Report the malaria status.
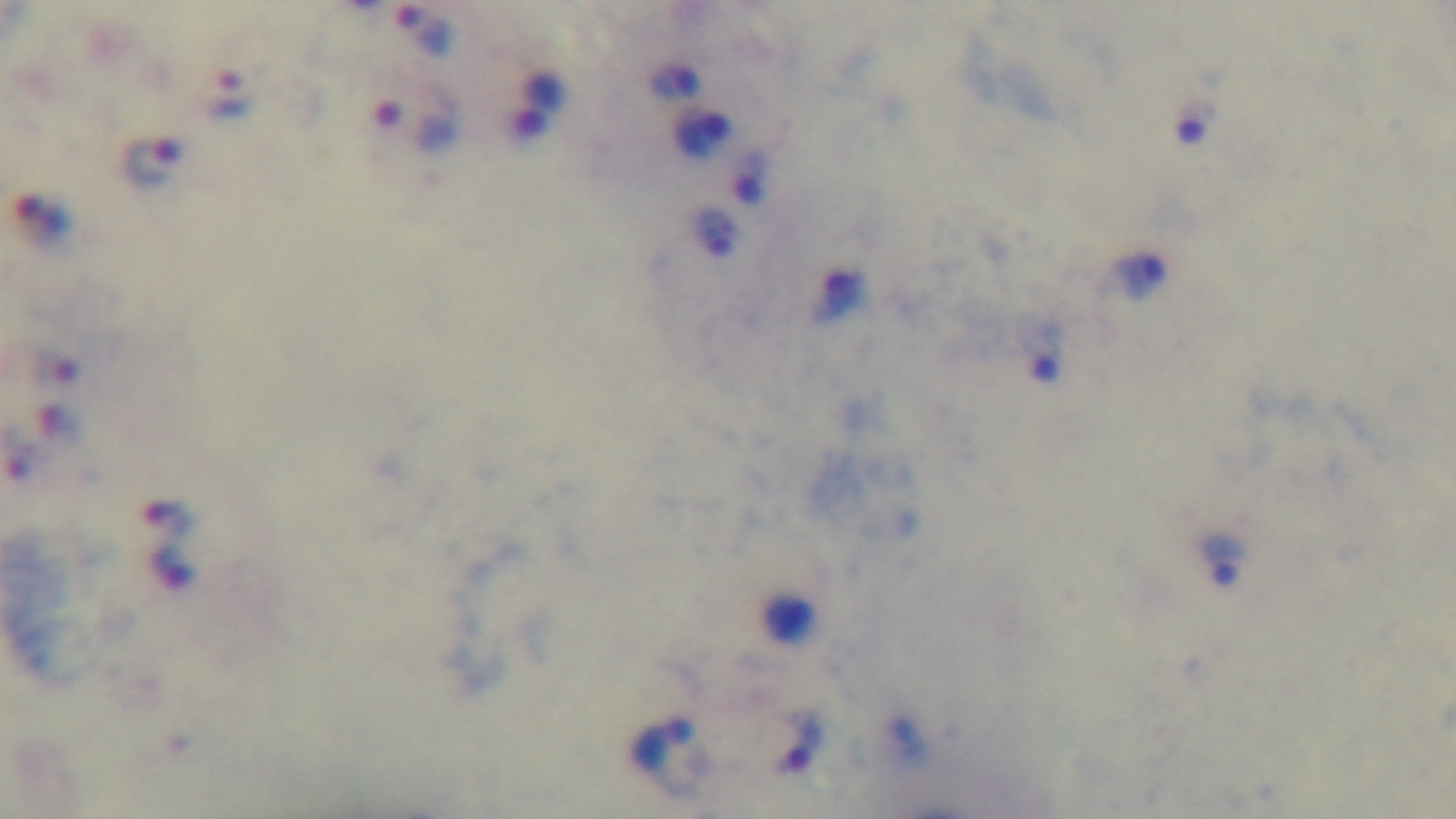

Infected.

stain = Giemsa
preparation = thick
capture = mounted 4K digital camera
modality = light microscopy
field of view = one from the slide
objective = 100x oil immersion